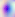

identification = Toxoplasma gondii
magnification = 400x
modality = photomicrograph